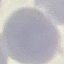

Summary:
  - Result: negative for malaria parasites
  - Capture: smartphone through the microscope eyepiece
  - Preparation: thin smear
  - Image type: cell patch, automatically extracted from a larger field of view and resized to 64 × 64 pixels
  - Stain: Giemsa